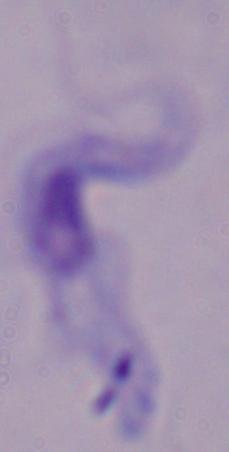

magnification = 1000x
identification = trypanosome
modality = photomicrograph